Give the position of every malaria parasite.
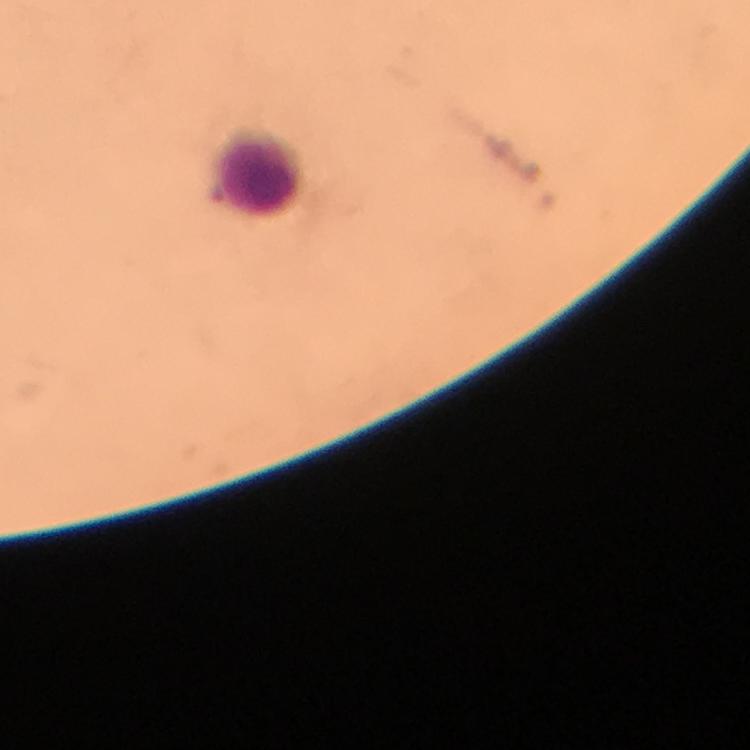
No malaria parasites detected.

Approximate object centers, in pixels from the top-left corner. Leukocyte locations: (x=256, y=171). Cropped region of a single field of view. Thick blood film. 100x magnification. Giemsa-stained preparation. From a malaria diagnostic workup. Image is 750×750 pixels. Immersion oil applied. Smartphone photograph taken through a microscope.